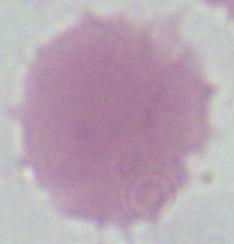

A red blood cell is seen. Micrograph. 1000x magnification.